Report the malaria status of this cell.
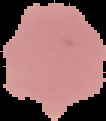
Uninfected.

Segmented cell region on a black background. Image is 106×121 pixels. From a thin blood smear.